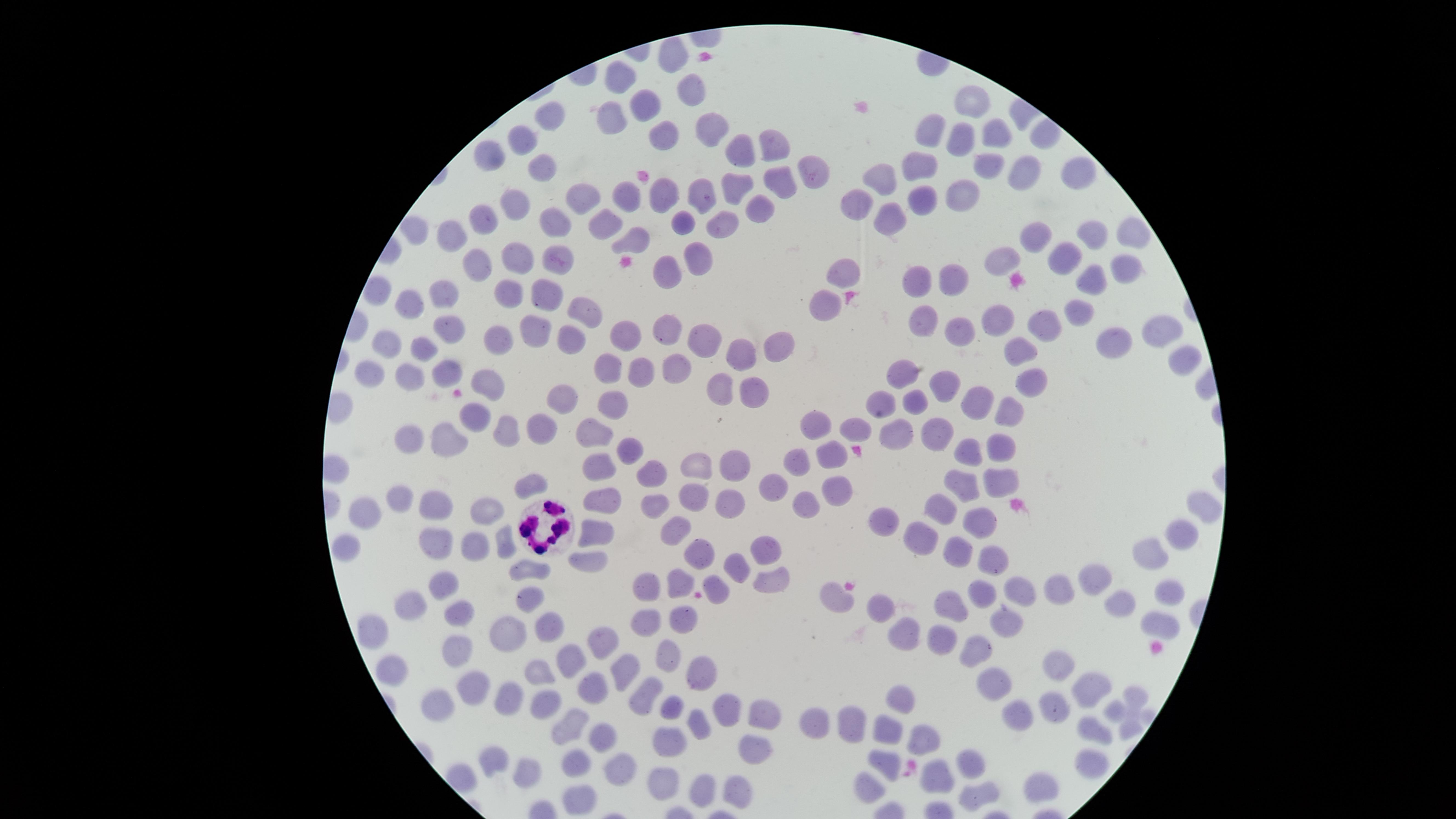

Approximate marker points as (x, y) in pixels.
Summary:
  - Uninfected red blood cells: (673, 56), (689, 79), (622, 82), (974, 105), (648, 109), (612, 117), (551, 120), (710, 123), (662, 132), (933, 132), (993, 136), (957, 139), (526, 141), (774, 148), (491, 153), (745, 153), (923, 165), (540, 166), (1078, 170), (814, 173), (1022, 176), (775, 178), (884, 179), (736, 184), (956, 193), (664, 194), (631, 196), (708, 196), (580, 198), (921, 198), (863, 201), (515, 208), (756, 208), (486, 217), (885, 218), (685, 221), (607, 222), (721, 222), (555, 224), (415, 228), (1086, 232), (453, 236), (1132, 236), (631, 240), (1037, 240), (522, 256), (1003, 257), (1062, 259), (553, 260), (695, 261), (480, 262), (1125, 266), (672, 269), (844, 273), (1088, 279), (951, 280), (924, 283), (378, 290), (548, 291), (510, 292), (442, 293), (410, 305), (827, 309), (586, 310), (1081, 310), (992, 316), (924, 323), (1049, 323), (663, 324), (1151, 330), (957, 332), (448, 333), (537, 333), (392, 338), (496, 340), (572, 340), (621, 340), (705, 340), (771, 345), (1117, 345), (1017, 347), (423, 352), (741, 352), (1177, 359), (675, 363), (610, 368), (904, 370), (642, 374), (408, 376), (368, 377), (444, 378), (1033, 380), (491, 381), (943, 385), (717, 390), (752, 390), (561, 396), (911, 399), (979, 399), (883, 401), (615, 406), (1010, 406), (476, 413), (541, 425), (816, 425), (511, 428), (854, 429), (938, 429), (897, 430), (411, 434), (597, 434), (452, 444), (998, 447), (629, 450), (967, 450), (835, 453), (736, 461), (700, 462), (799, 464), (597, 465), (649, 477), (530, 483), (776, 483), (1001, 483), (963, 487), (833, 491), (697, 493), (609, 499), (395, 501), (725, 501), (654, 502), (1199, 506), (435, 508), (367, 510), (806, 510), (942, 512), (488, 517), (890, 519), (981, 526), (674, 533), (1184, 534), (598, 536), (916, 540), (346, 546), (504, 547), (436, 548), (1155, 548), (766, 549), (480, 551), (957, 552), (699, 555), (989, 559), (590, 560), (741, 567), (530, 570), (1100, 578), (769, 582), (675, 584), (441, 585), (643, 587), (716, 587), (1060, 590), (1171, 590), (1021, 592), (982, 594), (530, 595), (841, 598), (956, 602), (417, 603), (1123, 604), (880, 607), (460, 609), (1006, 616), (644, 619), (553, 620), (684, 622), (1158, 622), (374, 627), (943, 639), (505, 641), (906, 642), (597, 645), (978, 647), (461, 653), (670, 656), (570, 658), (396, 666), (627, 668), (544, 673), (1057, 673), (701, 674), (996, 684), (475, 689), (592, 693), (645, 694), (1136, 696), (1086, 699), (504, 700), (544, 703), (906, 703), (1054, 703), (439, 704), (674, 706), (731, 706), (1115, 710), (758, 711), (855, 721), (819, 723), (702, 724), (573, 725), (1019, 725), (1129, 729), (891, 731), (1097, 733), (598, 736), (921, 743), (670, 747), (758, 754), (493, 760), (1093, 760), (577, 762), (616, 763), (886, 763), (970, 765), (533, 774), (666, 779), (938, 779), (1042, 784), (869, 786), (703, 789), (739, 790), (977, 794), (582, 800)
  - White blood cells: (554, 525)
  - Field of view: single
  - Preparation: thin smear of blood
  - Capture: smartphone photograph through the microscope eyepiece
  - Stain: Giemsa
  - Visible region: circular
  - Presence: no malaria parasites identified
  - Image size: 1456×819 pixels